Evaluate for malaria.
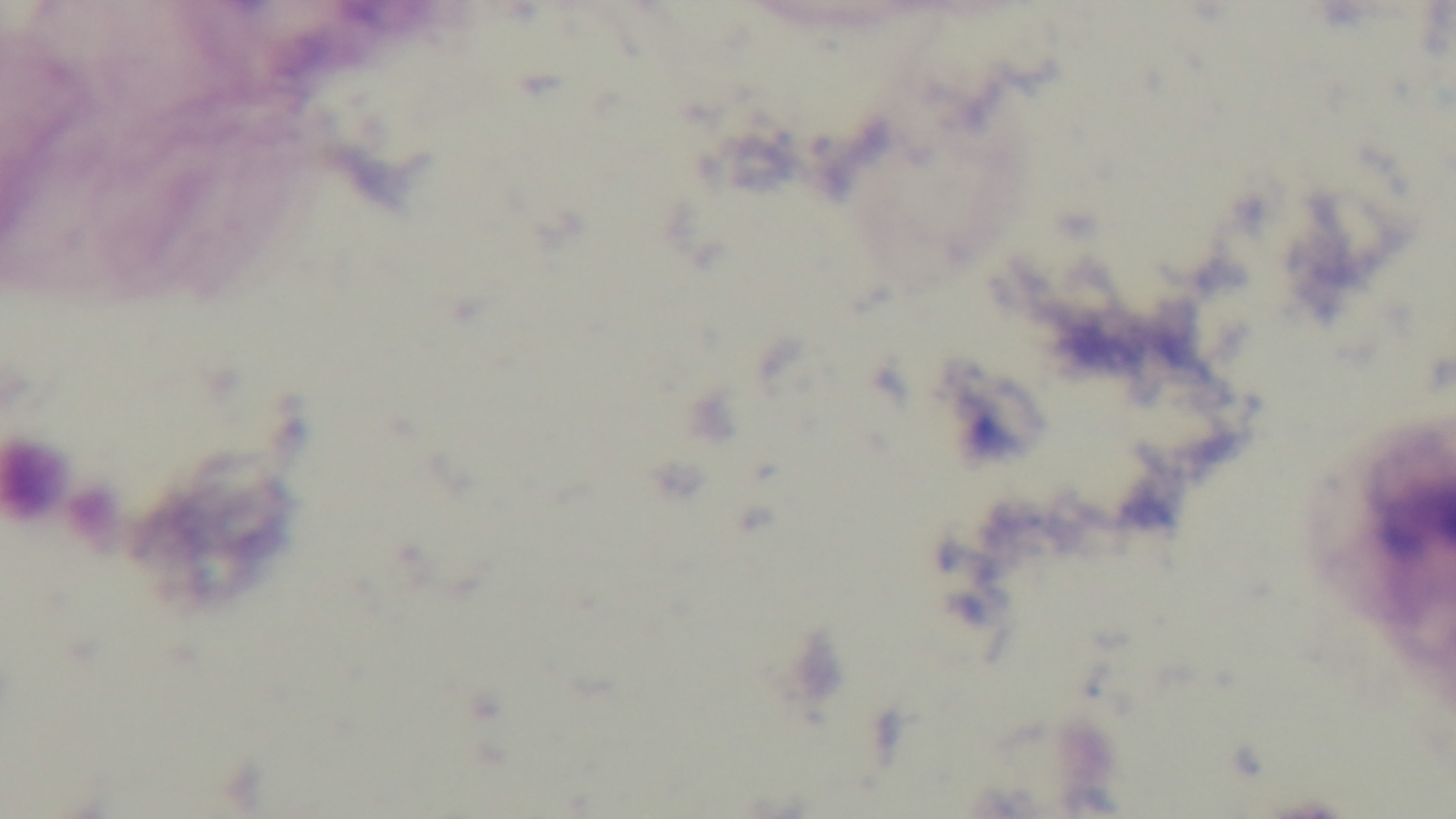

It is uninfected.

preparation = thick blood film
modality = light microscopy
stain = Giemsa
field of view = one from the slide
capture = mounted 4K digital camera
objective = 100x oil immersion